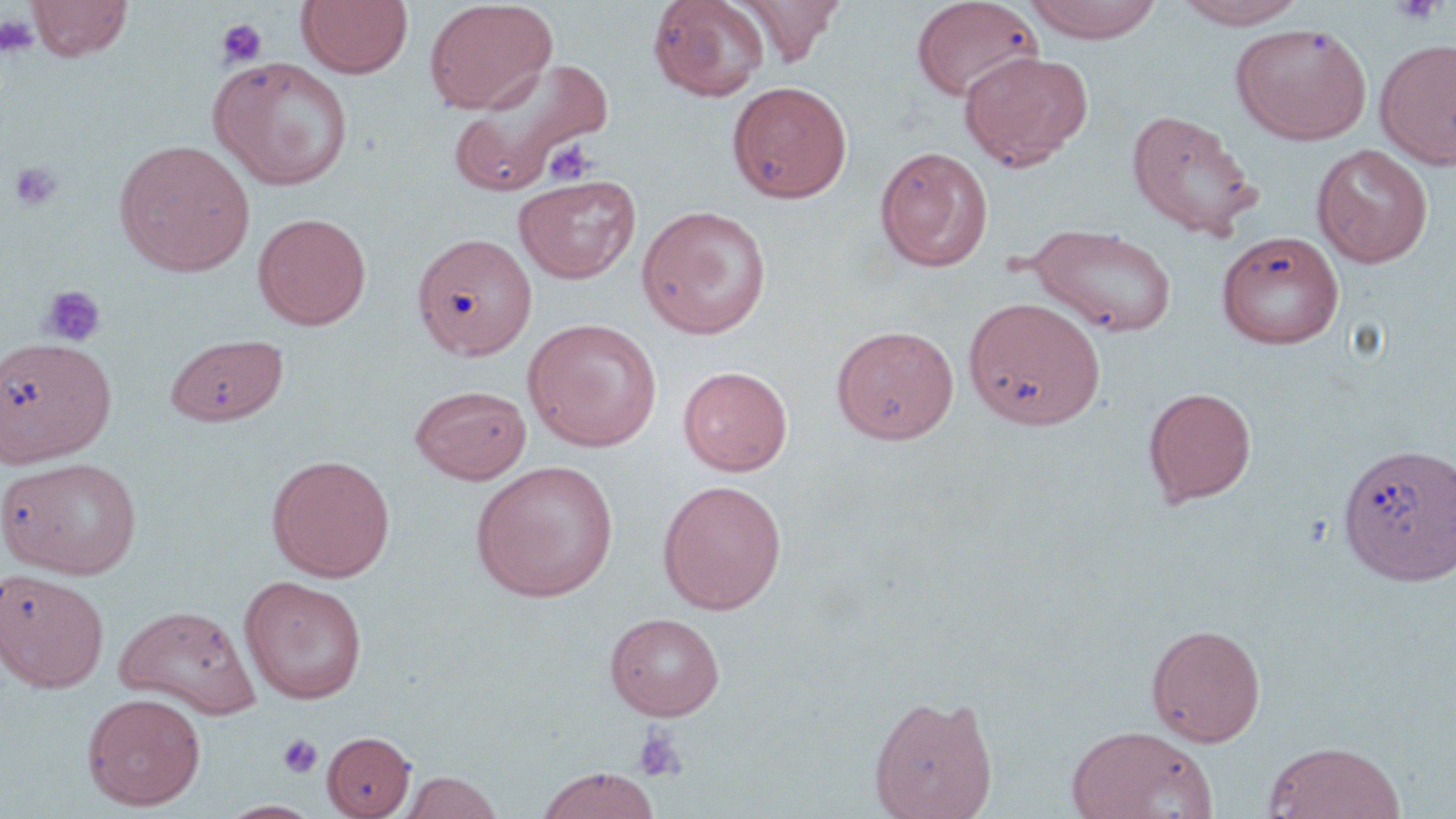

Summary:
  - Coordinate format: approximate bounding boxes as (x1,y1)-(x2,y2) corner pairs in pixels
  - Uninfected red blood cell locations: (27,0)-(133,61), (297,0)-(413,78), (424,0)-(557,114), (647,0)-(771,101), (732,0)-(845,66), (910,0)-(1043,102), (1021,0)-(1165,43), (1172,0)-(1307,29), (1230,22)-(1372,143), (1375,39)-(1456,169), (959,51)-(1093,170), (210,56)-(354,190), (450,56)-(614,195), (727,80)-(852,203), (1127,108)-(1259,239), (114,139)-(255,277), (1312,144)-(1433,268), (875,146)-(993,272), (513,173)-(641,284), (636,204)-(773,339), (253,211)-(371,330), (1026,223)-(1178,338), (1215,230)-(1345,349), (412,231)-(537,360), (963,295)-(1106,430), (523,318)-(663,452), (830,325)-(959,445), (165,333)-(289,426), (0,335)-(116,468), (678,365)-(793,476), (410,384)-(532,484), (1143,386)-(1257,507), (1336,442)-(1456,587), (266,454)-(395,581), (0,456)-(143,578), (470,460)-(619,602), (657,479)-(787,614), (0,569)-(110,692), (239,575)-(367,704), (113,605)-(260,718), (604,612)-(726,721), (1146,623)-(1267,747), (81,692)-(207,810), (868,693)-(999,818), (1065,725)-(1216,819), (322,730)-(416,818), (1262,741)-(1406,818), (534,766)-(662,818), (398,771)-(503,818)
  - Platelet locations: (1390,0)-(1446,25), (0,13)-(40,57), (216,18)-(268,69), (541,140)-(599,186), (9,161)-(64,213), (38,284)-(107,347), (632,724)-(688,784), (278,733)-(323,778)
  - Slide-level diagnosis: negative for blood parasites
  - Stain: May-Grünwald-Giemsa
  - Magnification: 1000x
  - Field of view: one of a larger specimen
  - Image size: 1456×819 pixels
  - Preparation: thin blood film
  - Modality: optical microscopy